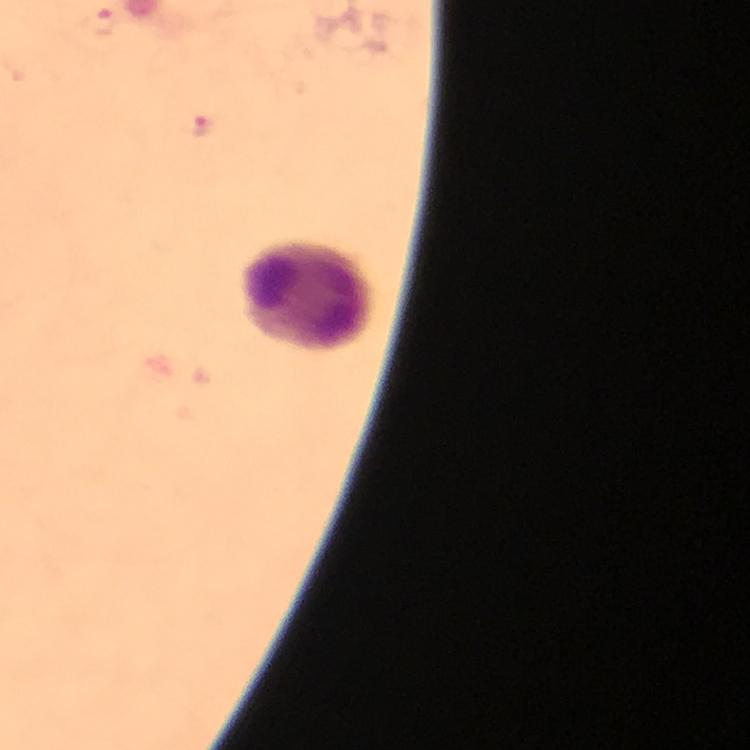

Approximate centers as [x, y] in pixels. Plasmodium parasite locations: [98, 23], [200, 127]. Leukocyte locations: [305, 296]. 100x magnification. A crop from one field of view. Thick smear. Immersion oil applied. Giemsa stain. Image is 750×750 pixels. From a malaria diagnostic workup. Photographed through the microscope with a smartphone camera.